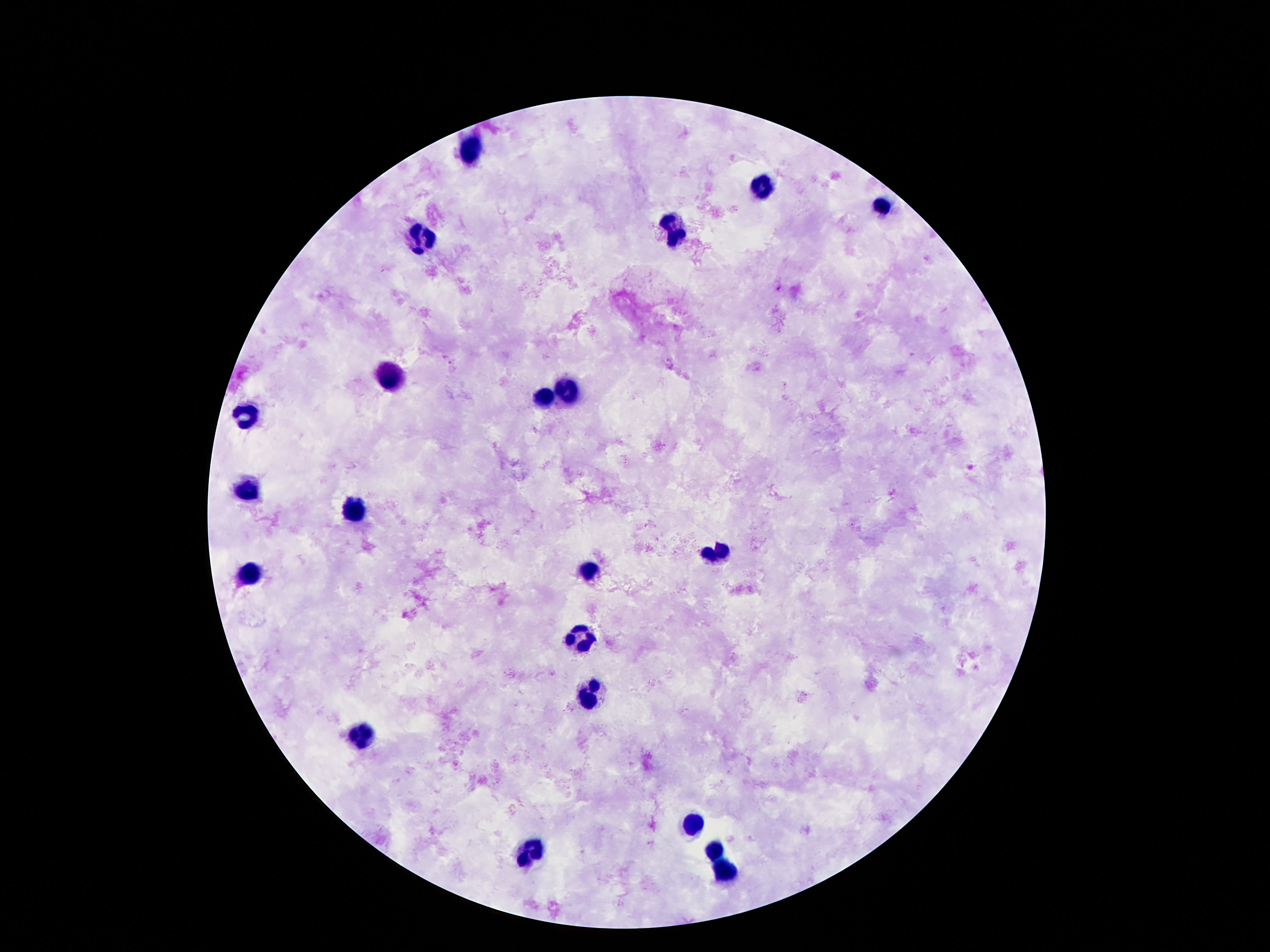

stain = Giemsa
image size = 1270×952 pixels
preparation = thick blood film
patient malaria status = uninfected
magnification = 100x
field of view = single
capture = smartphone camera through the microscope eyepiece
leukocyte locations = approximate object centers, in pixels from the top-left corner: (x=470, y=145), (x=764, y=187), (x=883, y=205), (x=671, y=233), (x=421, y=243), (x=388, y=375), (x=568, y=390), (x=543, y=398), (x=245, y=417), (x=247, y=493), (x=350, y=514), (x=715, y=549), (x=589, y=571), (x=249, y=575), (x=581, y=638), (x=591, y=695), (x=360, y=732), (x=694, y=821), (x=713, y=848), (x=533, y=854), (x=728, y=870)